Identify the parasite.
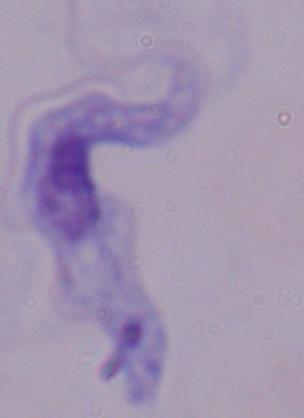

A trypanosome.

Photomicrograph. 1000x magnification.